Classify this cell by malaria status.
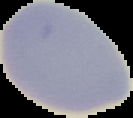
It is uninfected.

Summary:
  - Preparation: thin blood film
  - Image type: segmented cell region with the area outside set to black
  - Image size: 133×118 pixels